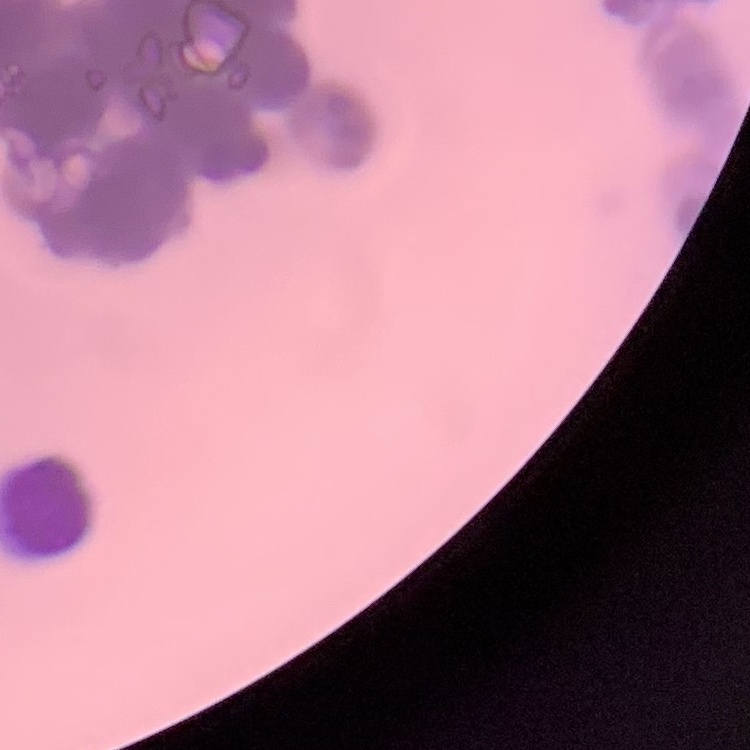

The erythrocytes exhibit rouleaux formation. Stained with either Field's or Giemsa. One tile cut from a larger photomicrograph. Thin blood smear.